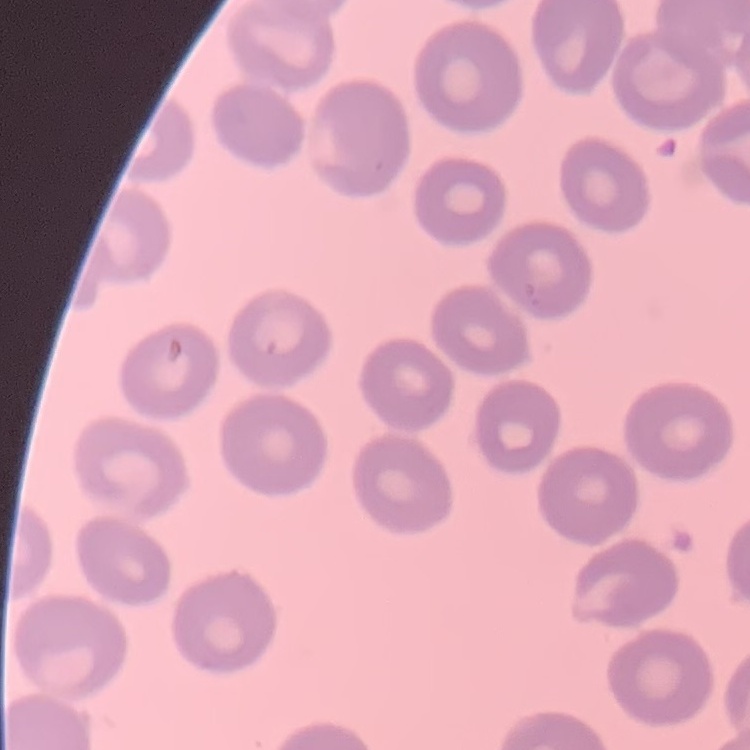
Summary:
  - Red blood cell morphology: no rouleaux formation
  - Preparation: thin peripheral smear
  - Image type: square crop of a larger photomicrograph
  - Stain: Field's or Giemsa